Identify the blood parasite species.
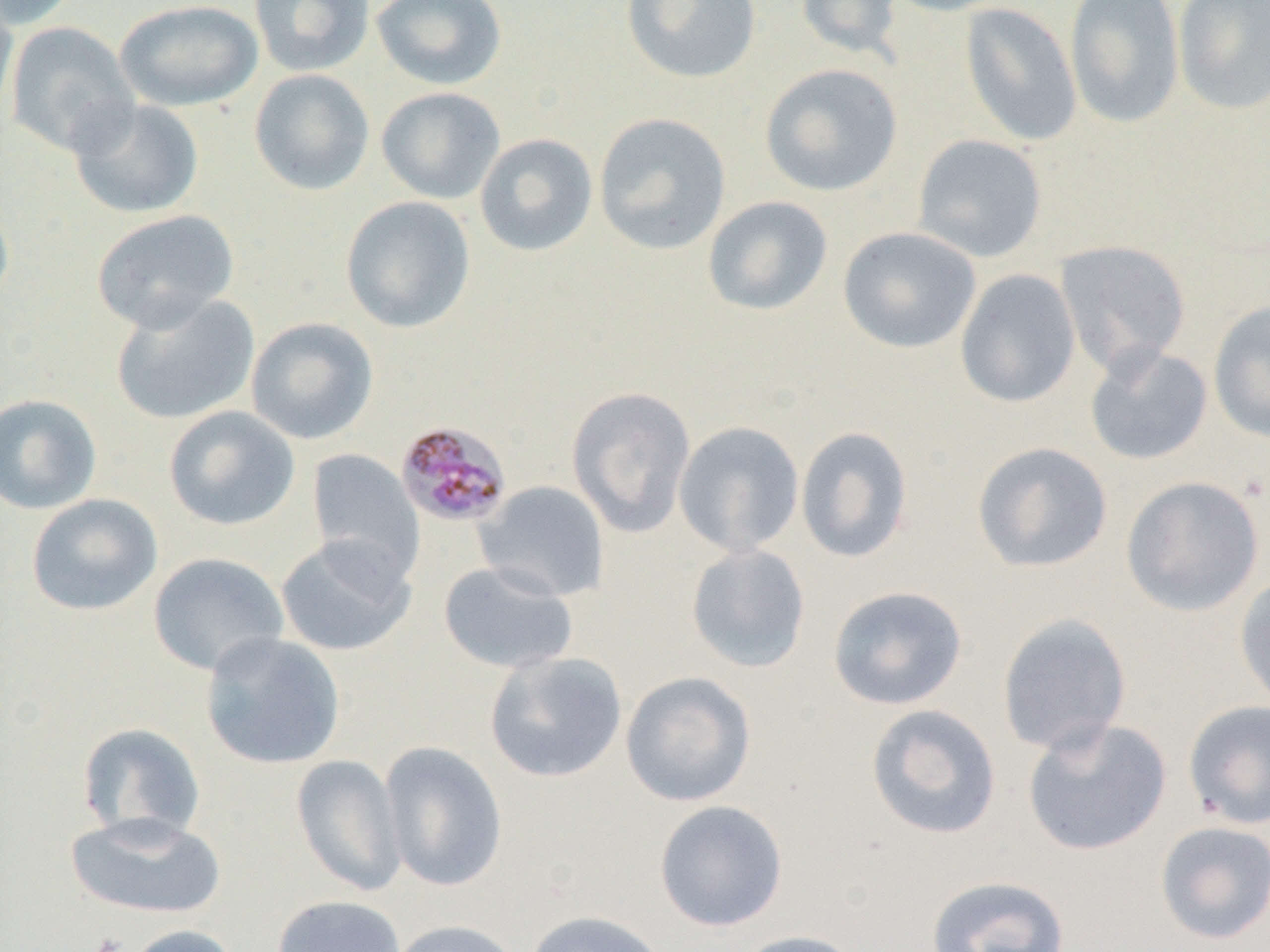
Plasmodium malariae.

Approximate bounding boxes as [x1, y1, x2, y2] in pixels. Plasmodium malariae-infected red blood cell locations: [395, 420, 513, 528]. Platelet locations: [90, 933, 128, 952]. Uninfected red blood cell locations: [0, 0, 82, 30], [114, 0, 263, 112], [249, 0, 375, 77], [370, 0, 508, 90], [621, 0, 761, 84], [794, 0, 905, 60], [880, 0, 1015, 16], [1065, 0, 1185, 129], [1173, 0, 1270, 115], [960, 2, 1083, 147], [0, 3, 18, 125], [5, 20, 140, 157], [759, 63, 903, 197], [249, 69, 375, 195], [375, 86, 506, 204], [67, 97, 204, 219], [593, 112, 731, 255], [474, 133, 598, 257], [912, 134, 1048, 262], [0, 192, 14, 310], [702, 195, 833, 316], [340, 196, 476, 333], [91, 209, 239, 333], [838, 226, 981, 353], [1054, 239, 1191, 377], [955, 268, 1081, 408], [111, 293, 260, 425], [1208, 300, 1270, 442], [245, 317, 379, 445], [1084, 344, 1213, 465], [566, 386, 696, 537], [0, 393, 102, 515], [164, 405, 300, 531], [673, 421, 805, 557], [795, 426, 914, 564], [971, 441, 1113, 573], [306, 448, 425, 583], [1121, 475, 1265, 617], [473, 480, 610, 603], [26, 493, 163, 616], [275, 535, 417, 657], [685, 543, 811, 673], [148, 552, 289, 676], [438, 561, 579, 674], [1234, 573, 1270, 712], [827, 585, 968, 710], [997, 613, 1132, 757], [200, 631, 345, 770], [484, 651, 627, 783], [620, 671, 757, 807], [1182, 700, 1270, 830], [865, 704, 1002, 839], [1021, 717, 1172, 856], [77, 722, 206, 844], [378, 740, 508, 891], [291, 754, 407, 897], [654, 800, 788, 931], [64, 811, 227, 920], [1155, 821, 1270, 945], [925, 874, 1071, 952], [271, 894, 407, 952], [522, 909, 670, 952], [389, 919, 526, 952], [122, 924, 242, 952], [729, 929, 868, 952]. 1000x magnification. Thin blood smear. Optical microscopy. Single field of view. Image is 1270×952 pixels.